Assess the morphology of the red blood cells.
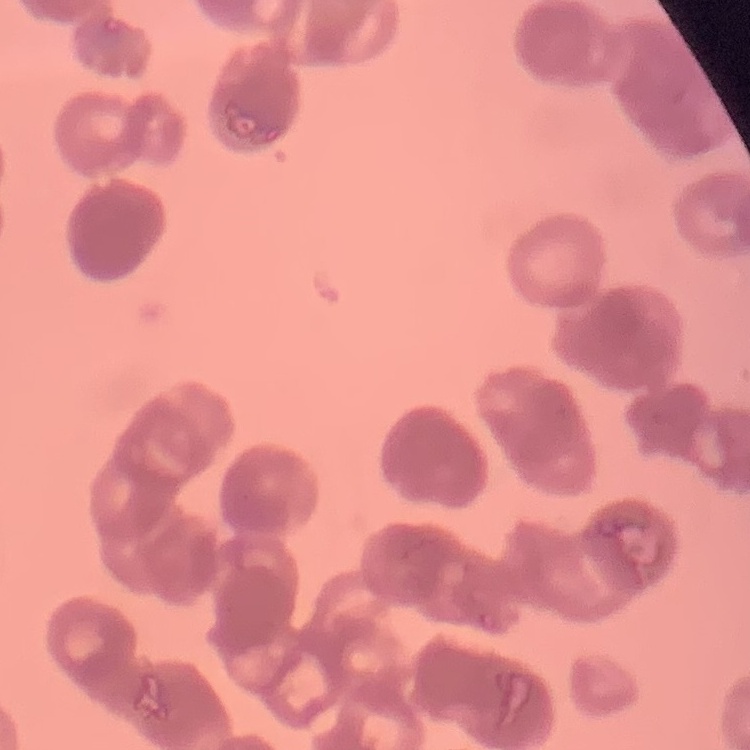

They show rouleaux formation.

preparation = thin blood smear
stain = Field's or Giemsa
image type = square crop of a larger photomicrograph